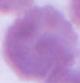
Photomicrograph. Captured at 1000x magnification. A red blood cell is shown.